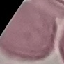

malaria status = uninfected
capture = smartphone camera at the microscope eyepiece
image type = automatically extracted cell patch, resized to 64 × 64 pixels
stain = Giemsa
preparation = thin smear